Name the parasite shown.
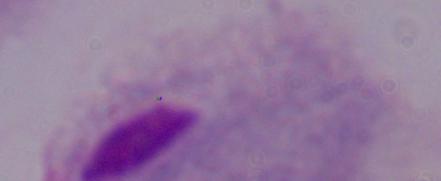
A trichomonad.

Photomicrograph. 1000x magnification.